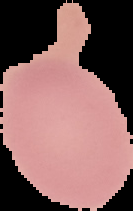
image size = 133×211 pixels
result = no malaria parasites seen
preparation = thin blood film
image type = segmented cell region on a black background